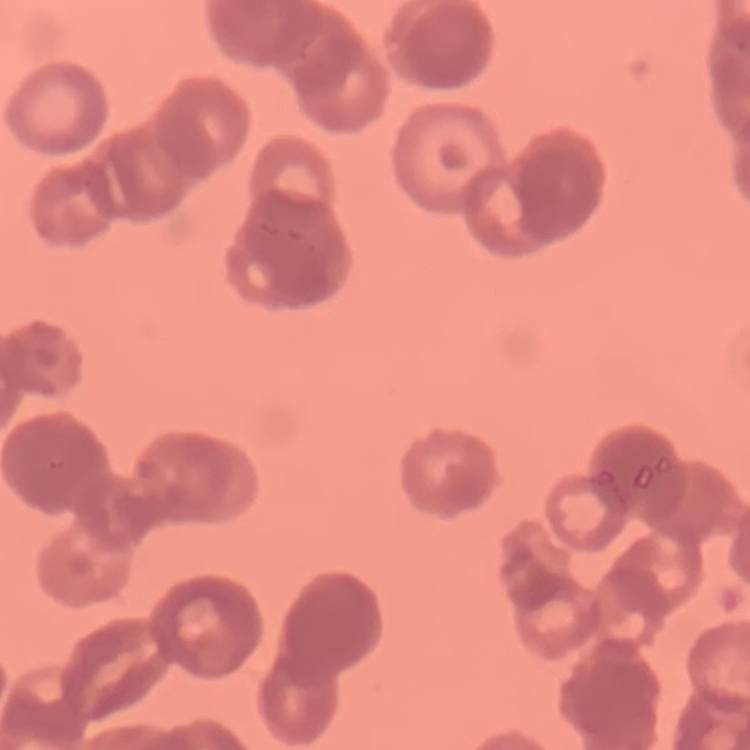
The red blood cells exhibit rouleaux formation. Field's or Giemsa stain. Thin blood smear. Square crop of a larger photomicrograph.